Report the malaria status of this cell.
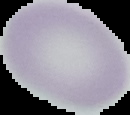
Uninfected.

Image is 130×115 pixels. From a thin blood smear. Segmented cell region on a black background.